Evaluate for Plasmodium parasites.
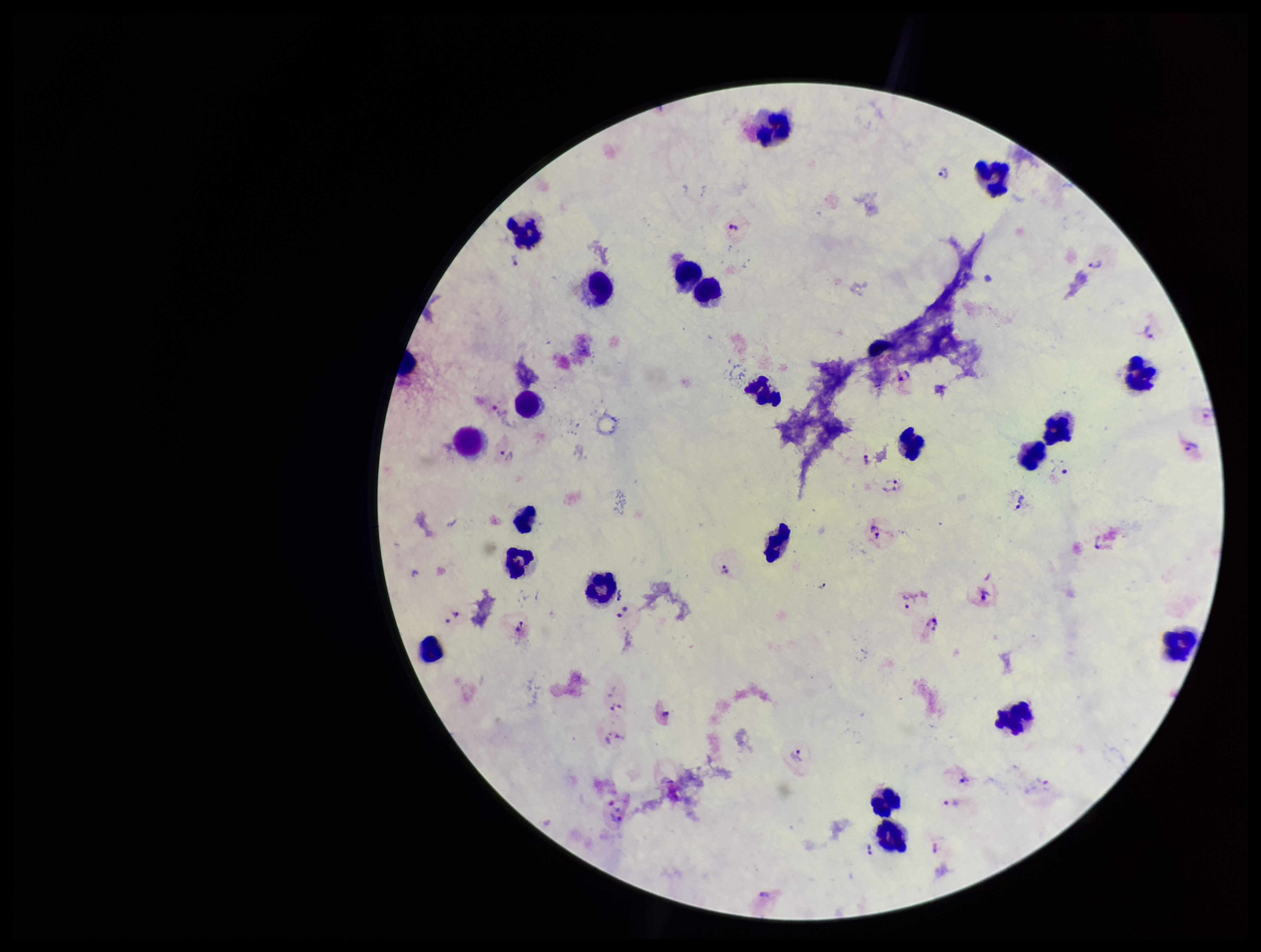
Seen.

Summary:
  - Image size: 1261×952 pixels
  - Species reported for this patient: Plasmodium vivax
  - Stain: Giemsa
  - Patient malaria status: positive
  - Preparation: thick smear
  - Parasite count: 24
  - Field of view: single
  - Leukocyte count: 24
  - Capture: smartphone photograph through the microscope eyepiece